Name the blood parasite species.
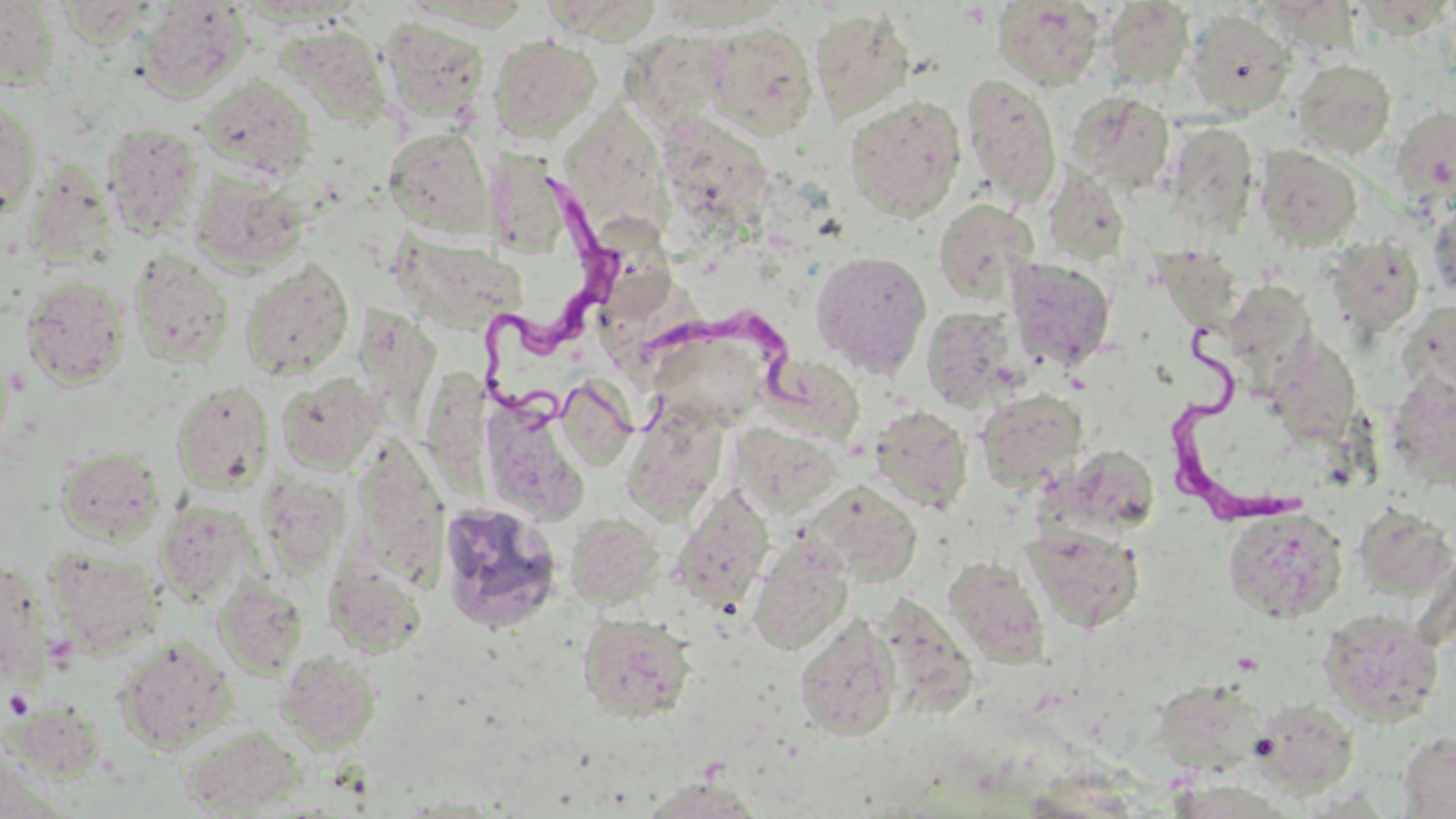

Trypanosoma brucei.

Approximate bounding boxes as [x1, y1, x2, y2] in pixels. Trypanosoma brucei locations: [477, 167, 623, 416], [641, 307, 831, 431], [1161, 328, 1306, 528]. Platelet locations: [4, 689, 34, 720]. Uninfected red blood cell locations: [0, 0, 62, 90], [138, 1, 251, 101], [993, 1, 1105, 90], [1104, 1, 1195, 90], [551, 5, 673, 56], [810, 8, 916, 121], [1187, 9, 1295, 119], [379, 17, 491, 124], [701, 22, 819, 138], [277, 23, 392, 128], [488, 34, 602, 143], [633, 39, 744, 139], [1292, 58, 1397, 158], [961, 73, 1061, 207], [197, 75, 316, 180], [0, 91, 42, 223], [1067, 91, 1176, 193], [844, 95, 966, 221], [562, 101, 681, 225], [1391, 105, 1456, 208], [101, 121, 205, 240], [1160, 121, 1260, 239], [383, 127, 497, 237], [676, 128, 772, 238], [1256, 146, 1363, 250], [25, 161, 118, 269], [1042, 166, 1129, 268], [191, 171, 309, 272], [933, 198, 1038, 304], [1428, 199, 1456, 302], [602, 215, 684, 320], [391, 232, 527, 333], [1324, 236, 1425, 336], [128, 250, 235, 367], [810, 250, 931, 378], [1162, 251, 1251, 347], [1005, 257, 1117, 371], [240, 259, 355, 378], [20, 274, 130, 389], [602, 279, 719, 372], [1244, 286, 1321, 403], [1398, 300, 1456, 400], [357, 306, 445, 443], [921, 306, 1024, 409], [647, 335, 766, 433], [1294, 346, 1361, 469], [788, 366, 858, 448], [433, 369, 524, 510], [276, 372, 386, 474], [554, 376, 637, 470], [1387, 376, 1456, 491], [171, 379, 275, 494], [976, 389, 1087, 492], [621, 402, 728, 522], [487, 403, 597, 510], [870, 406, 972, 511], [730, 423, 844, 517], [1059, 444, 1160, 535], [55, 446, 166, 543], [258, 476, 350, 578], [802, 480, 923, 587], [670, 485, 774, 613], [437, 499, 561, 633], [157, 503, 256, 604], [1223, 506, 1348, 622], [1353, 506, 1456, 598], [565, 513, 662, 608], [1024, 524, 1144, 632], [748, 539, 853, 655], [43, 547, 165, 656], [944, 555, 1048, 666], [324, 563, 429, 659], [214, 576, 308, 677], [875, 592, 978, 719], [1318, 608, 1445, 724], [578, 612, 698, 723], [795, 612, 901, 741], [114, 637, 236, 751], [277, 650, 380, 750], [1157, 675, 1276, 770], [1250, 698, 1359, 797], [8, 700, 107, 783], [180, 725, 307, 815], [1398, 730, 1456, 818], [641, 777, 766, 818]. 1000x magnification. Thin blood smear. Optical microscopy. May-Grünwald-Giemsa stain. Image is 1456×819 pixels. Single field of view.